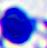
A leukocyte is shown. Micrograph. 400x magnification.